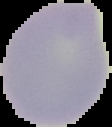

preparation = thin blood film
image size = 112×127 pixels
malaria status = uninfected
image type = cell region segmented out of the field of view; surrounding area masked to black